Report the malaria status.
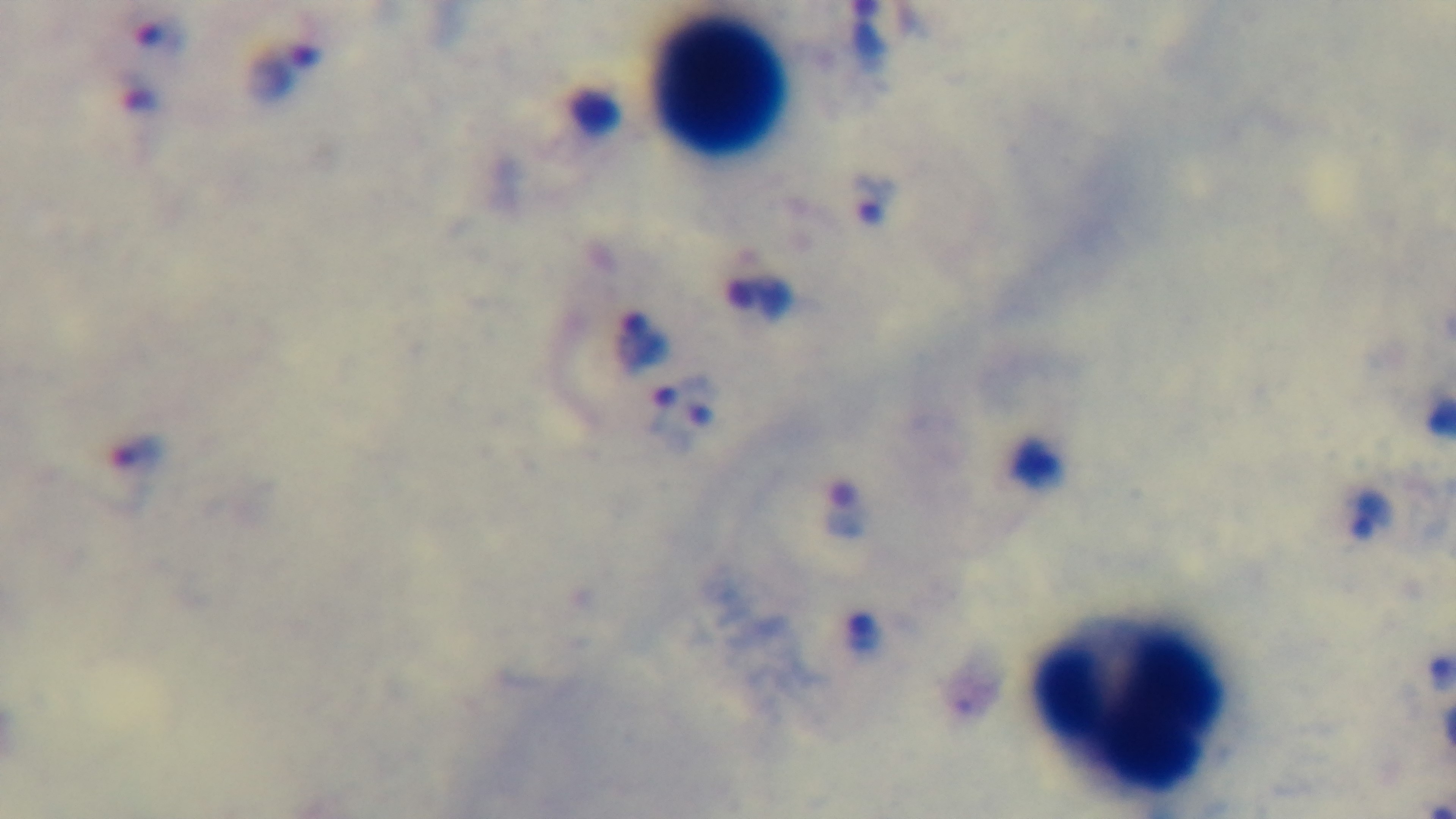

Infected.

{
  "preparation": "thick",
  "modality": "light microscopy",
  "field_of_view": "single",
  "objective": "100x oil immersion",
  "capture": "mounted 4K digital camera",
  "stain": "Giemsa"
}